Outline each Plasmodium falciparum-infected red blood cell.
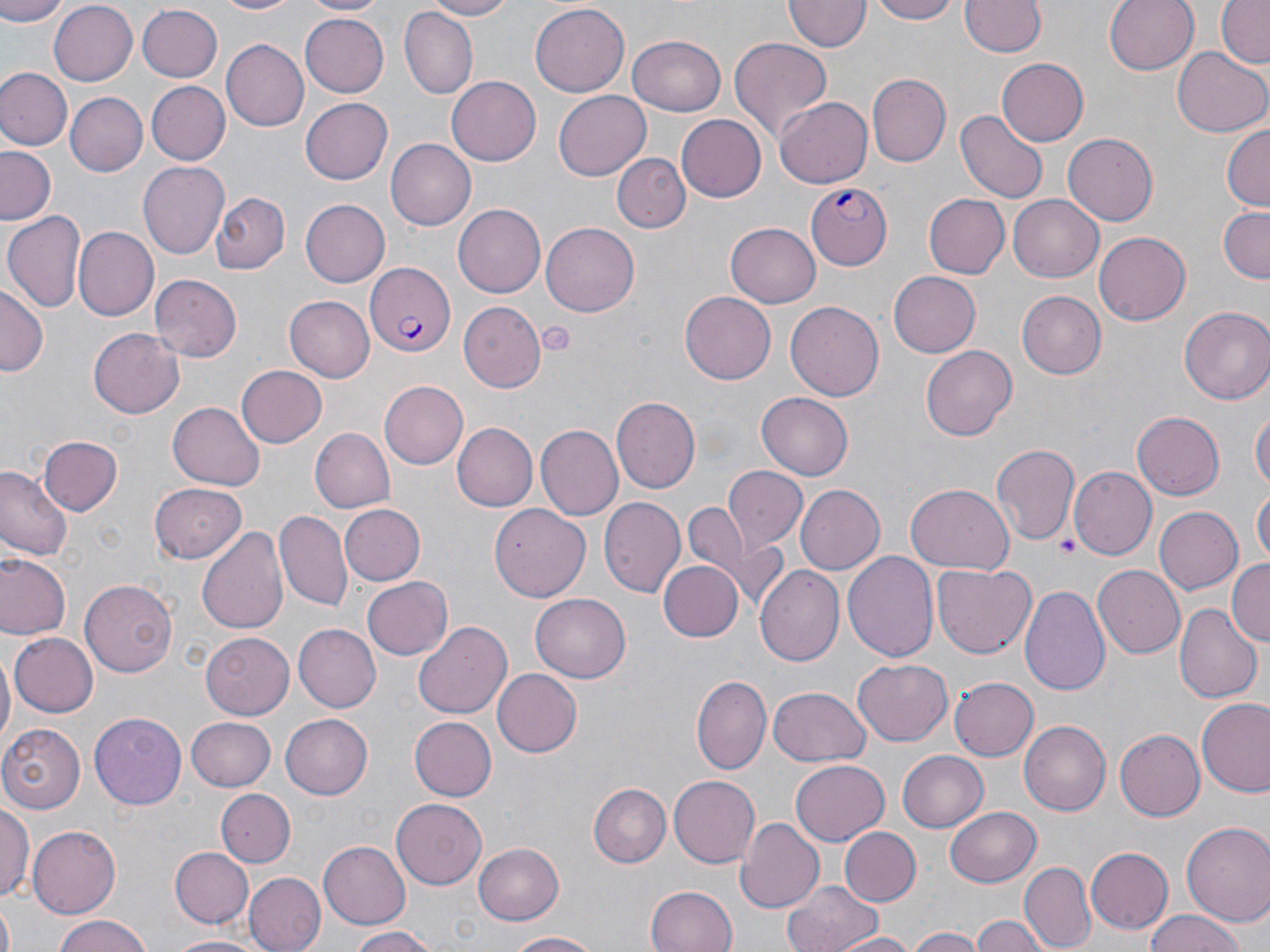

Approximate bounding boxes as named x1/y1/x2/y2 corners in pixels.
Plasmodium falciparum-infected red blood cells: (x1=806, y1=184, x2=893, y2=267), (x1=362, y1=264, x2=455, y2=355).

slide_level_diagnosis: Plasmodium falciparum
platelet_locations: 'approximate bounding boxes as named x1/y1/x2/y2 corners in pixels: (x1=537, y1=321, x2=576, y2=357), (x1=1056, y1=535, x2=1079, y2=556)'
stain: May-Grünwald-Giemsa
uninfected_red_blood_cell_locations: 'approximate bounding boxes as named x1/y1/x2/y2 corners in pixels: (x1=0, y1=0, x2=69, y2=23), (x1=213, y1=0, x2=303, y2=16), (x1=302, y1=0, x2=387, y2=16), (x1=420, y1=0, x2=517, y2=20), (x1=865, y1=0, x2=963, y2=24), (x1=1104, y1=0, x2=1199, y2=76), (x1=1215, y1=0, x2=1270, y2=68), (x1=47, y1=1, x2=137, y2=85), (x1=961, y1=1, x2=1045, y2=58), (x1=783, y1=2, x2=867, y2=53), (x1=530, y1=4, x2=629, y2=97), (x1=137, y1=5, x2=224, y2=82), (x1=399, y1=8, x2=477, y2=101), (x1=299, y1=12, x2=388, y2=96), (x1=627, y1=36, x2=724, y2=116), (x1=729, y1=37, x2=834, y2=143), (x1=220, y1=39, x2=307, y2=132), (x1=1172, y1=47, x2=1267, y2=138), (x1=996, y1=58, x2=1089, y2=146), (x1=0, y1=67, x2=72, y2=149), (x1=447, y1=74, x2=544, y2=167), (x1=868, y1=74, x2=951, y2=166), (x1=146, y1=80, x2=229, y2=165), (x1=552, y1=91, x2=651, y2=179), (x1=66, y1=93, x2=146, y2=175), (x1=300, y1=97, x2=393, y2=185), (x1=774, y1=97, x2=873, y2=187), (x1=954, y1=110, x2=1047, y2=204), (x1=676, y1=113, x2=766, y2=200), (x1=1222, y1=125, x2=1269, y2=212), (x1=1062, y1=131, x2=1160, y2=226), (x1=388, y1=138, x2=477, y2=231), (x1=0, y1=148, x2=59, y2=225), (x1=614, y1=152, x2=690, y2=232), (x1=138, y1=161, x2=228, y2=259), (x1=209, y1=193, x2=289, y2=274), (x1=922, y1=194, x2=1009, y2=279), (x1=1009, y1=194, x2=1104, y2=280), (x1=299, y1=200, x2=390, y2=287), (x1=452, y1=202, x2=546, y2=295), (x1=1215, y1=206, x2=1270, y2=283), (x1=4, y1=210, x2=88, y2=315), (x1=724, y1=223, x2=819, y2=307), (x1=542, y1=224, x2=639, y2=315), (x1=74, y1=229, x2=158, y2=322), (x1=1093, y1=230, x2=1191, y2=326), (x1=889, y1=272, x2=981, y2=357), (x1=151, y1=274, x2=243, y2=359), (x1=0, y1=286, x2=46, y2=378), (x1=679, y1=291, x2=775, y2=385), (x1=1017, y1=292, x2=1105, y2=378), (x1=283, y1=295, x2=373, y2=382), (x1=786, y1=300, x2=884, y2=401), (x1=459, y1=302, x2=544, y2=389), (x1=1180, y1=306, x2=1270, y2=404), (x1=89, y1=327, x2=183, y2=418), (x1=921, y1=347, x2=1017, y2=439), (x1=237, y1=365, x2=327, y2=448), (x1=377, y1=381, x2=467, y2=469), (x1=757, y1=392, x2=852, y2=479), (x1=613, y1=397, x2=700, y2=493), (x1=169, y1=401, x2=264, y2=488), (x1=1251, y1=403, x2=1269, y2=500), (x1=1132, y1=411, x2=1225, y2=501), (x1=455, y1=422, x2=537, y2=512), (x1=535, y1=426, x2=622, y2=521), (x1=310, y1=428, x2=395, y2=512), (x1=40, y1=436, x2=123, y2=515), (x1=992, y1=445, x2=1081, y2=546), (x1=724, y1=466, x2=806, y2=550), (x1=0, y1=467, x2=71, y2=563), (x1=1071, y1=468, x2=1154, y2=558), (x1=149, y1=482, x2=246, y2=565), (x1=797, y1=484, x2=884, y2=576), (x1=905, y1=484, x2=1014, y2=572), (x1=1252, y1=487, x2=1270, y2=563), (x1=599, y1=498, x2=685, y2=598), (x1=683, y1=500, x2=751, y2=580), (x1=338, y1=504, x2=424, y2=585), (x1=487, y1=505, x2=591, y2=601), (x1=1153, y1=506, x2=1244, y2=596), (x1=275, y1=510, x2=351, y2=612), (x1=199, y1=526, x2=290, y2=637), (x1=844, y1=550, x2=939, y2=661), (x1=2, y1=555, x2=70, y2=640), (x1=658, y1=559, x2=744, y2=642), (x1=1227, y1=559, x2=1270, y2=646), (x1=932, y1=561, x2=1037, y2=659), (x1=756, y1=564, x2=845, y2=667), (x1=1093, y1=564, x2=1187, y2=657), (x1=360, y1=575, x2=452, y2=661), (x1=81, y1=578, x2=181, y2=676), (x1=1022, y1=584, x2=1112, y2=697), (x1=531, y1=592, x2=631, y2=682), (x1=1175, y1=605, x2=1260, y2=704), (x1=415, y1=623, x2=511, y2=719), (x1=294, y1=624, x2=381, y2=711), (x1=201, y1=632, x2=294, y2=719), (x1=9, y1=633, x2=98, y2=716), (x1=0, y1=648, x2=14, y2=756), (x1=852, y1=660, x2=952, y2=746), (x1=494, y1=670, x2=581, y2=756), (x1=693, y1=675, x2=769, y2=774), (x1=949, y1=675, x2=1039, y2=761), (x1=768, y1=685, x2=869, y2=766), (x1=1198, y1=698, x2=1270, y2=797), (x1=279, y1=712, x2=371, y2=799), (x1=90, y1=713, x2=186, y2=809), (x1=185, y1=715, x2=277, y2=789), (x1=408, y1=716, x2=496, y2=801), (x1=1019, y1=721, x2=1110, y2=815), (x1=1, y1=724, x2=86, y2=811), (x1=1114, y1=730, x2=1204, y2=820), (x1=898, y1=749, x2=988, y2=833), (x1=790, y1=760, x2=890, y2=846), (x1=669, y1=775, x2=760, y2=867), (x1=588, y1=783, x2=669, y2=868), (x1=218, y1=789, x2=295, y2=866), (x1=390, y1=800, x2=486, y2=888), (x1=0, y1=801, x2=34, y2=905), (x1=947, y1=807, x2=1040, y2=887), (x1=737, y1=817, x2=825, y2=912), (x1=1181, y1=820, x2=1270, y2=926), (x1=27, y1=826, x2=119, y2=919), (x1=838, y1=827, x2=921, y2=907), (x1=475, y1=841, x2=563, y2=924), (x1=317, y1=842, x2=412, y2=926), (x1=171, y1=847, x2=254, y2=929), (x1=1085, y1=848, x2=1174, y2=932), (x1=1020, y1=861, x2=1095, y2=951), (x1=244, y1=874, x2=325, y2=952), (x1=784, y1=878, x2=882, y2=952), (x1=644, y1=885, x2=738, y2=952), (x1=1144, y1=912, x2=1250, y2=952), (x1=971, y1=914, x2=1052, y2=952), (x1=49, y1=915, x2=157, y2=952), (x1=344, y1=926, x2=439, y2=952), (x1=906, y1=928, x2=985, y2=952), (x1=505, y1=931, x2=604, y2=951), (x1=836, y1=932, x2=917, y2=952), (x1=163, y1=934, x2=270, y2=952)'
magnification: 1000x
image_size: 1270×952 pixels
preparation: thin blood smear
modality: light microscopy
field_of_view: one of a larger specimen